State which parasite is depicted.
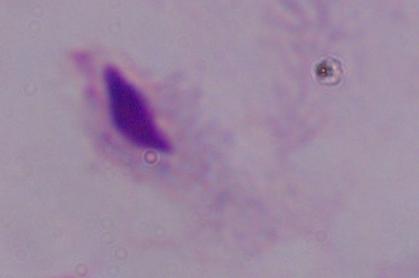

A trichomonad.

Summary:
  - Modality: photomicrograph
  - Magnification: 1000x